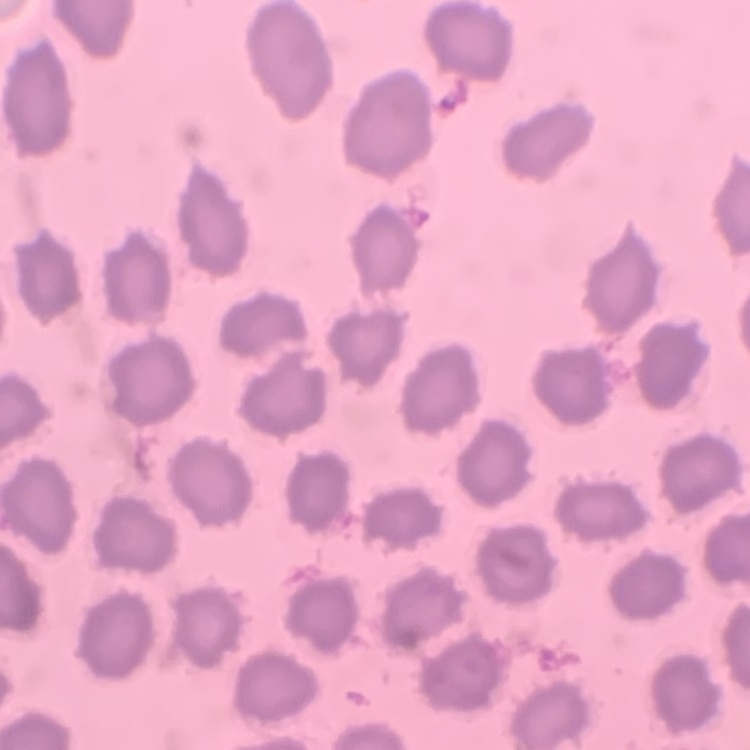 The erythrocytes exhibit no rouleaux formation. Thin blood film. Field's or Giemsa stain. One tile cut from a larger photomicrograph.